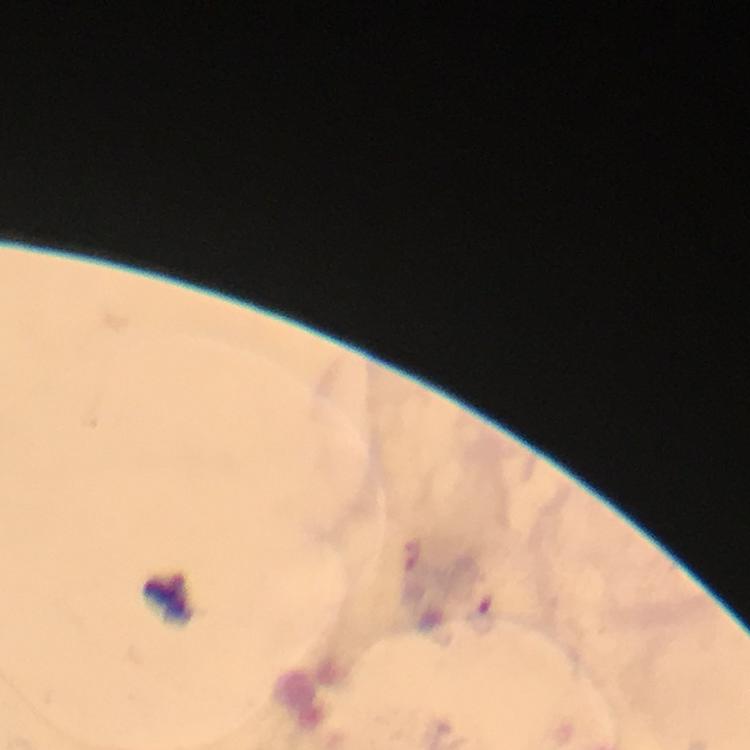
leukocyte locations = approximate centers as (x, y) in pixels: (171, 598)
context = from a malaria diagnostic workup
immersion oil = applied
malaria parasites = none detected
image size = 750×750 pixels
stain = Giemsa
magnification = 100x
cropped from = a single field of view
preparation = thick smear
capture = smartphone mounted on the microscope